Identify the parasite.
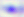
Toxoplasma gondii.

Photomicrograph. 400x magnification.